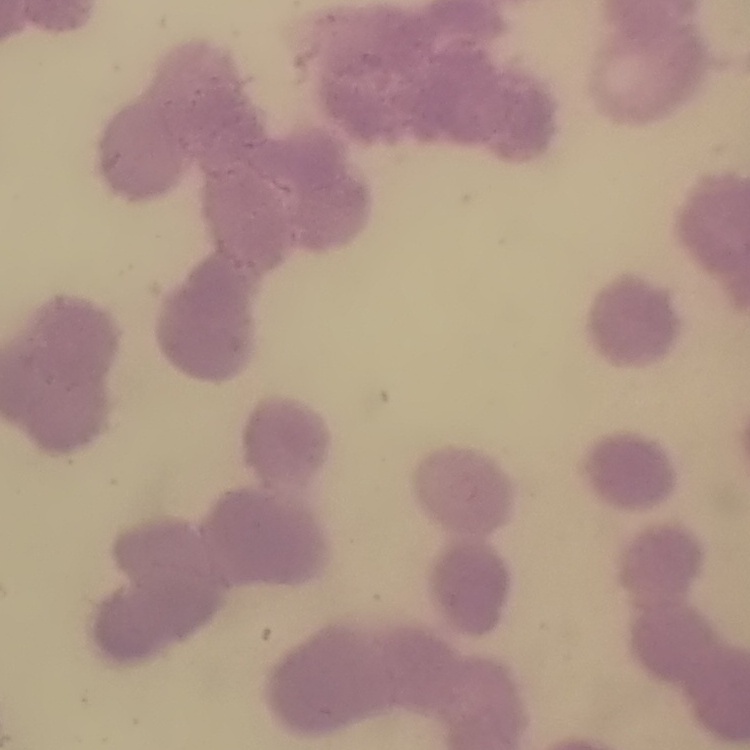

The red blood cells show rouleaux formation. Stained with either Field's or Giemsa. Square crop of a larger photomicrograph. Thin peripheral smear.